Give the position of every leukocyte visible.
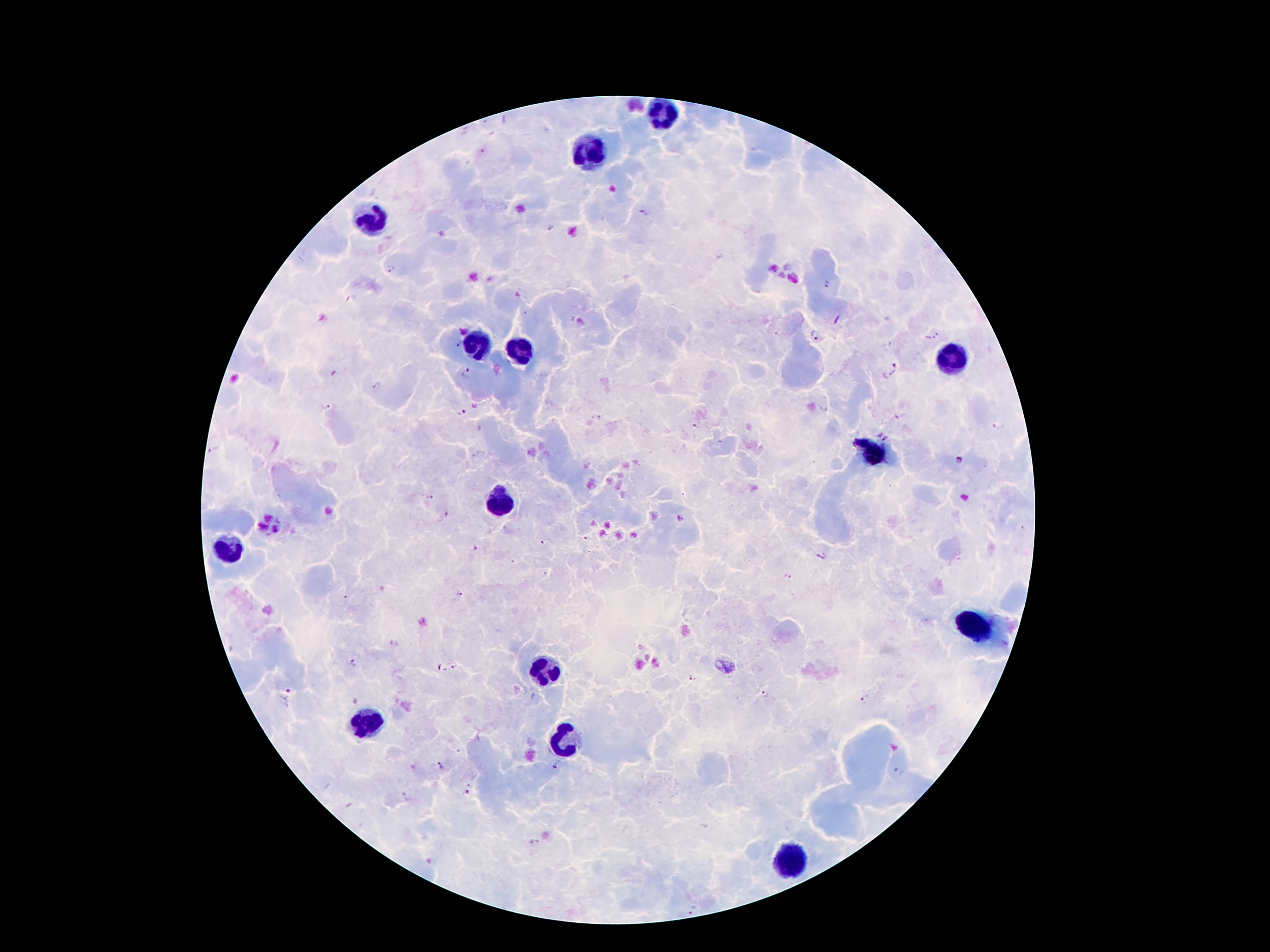

Approximate centers as {x, y} in pixels.
Leukocytes: {661, 114}, {589, 154}, {365, 217}, {474, 343}, {518, 351}, {944, 360}, {873, 454}, {495, 500}, {226, 548}, {976, 624}, {545, 672}, {367, 725}, {564, 742}, {793, 859}.

Plasmodium parasite locations: {643, 212}, {390, 268}, {827, 284}, {937, 334}, {815, 335}, {458, 345}, {896, 364}, {466, 373}, {378, 387}, {324, 406}, {824, 409}, {461, 413}, {999, 424}, {696, 427}, {883, 436}, {214, 450}, {961, 460}, {431, 498}, {446, 514}, {584, 539}, {544, 543}, {475, 548}, {789, 576}, {460, 595}, {355, 663}, {454, 665}, {439, 669}, {694, 678}, {289, 689}, {762, 694}, {864, 698}, {441, 766}, {557, 766}, {899, 771}, {467, 789}, {534, 842}, {692, 911}. Thick blood smear. One field from this slide. Image is 1270×952 pixels. 100x magnification. Photographed through the microscope eyepiece with a smartphone camera. Giemsa stain. Patient malaria status: infected with Plasmodium falciparum.